Assess this cell for malaria.
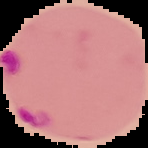

It is parasitized.

image_type: segmented cell region with the area outside set to black
image_size: 148×148 pixels
preparation: thin blood film